Locate leukocytes (white blood cells).
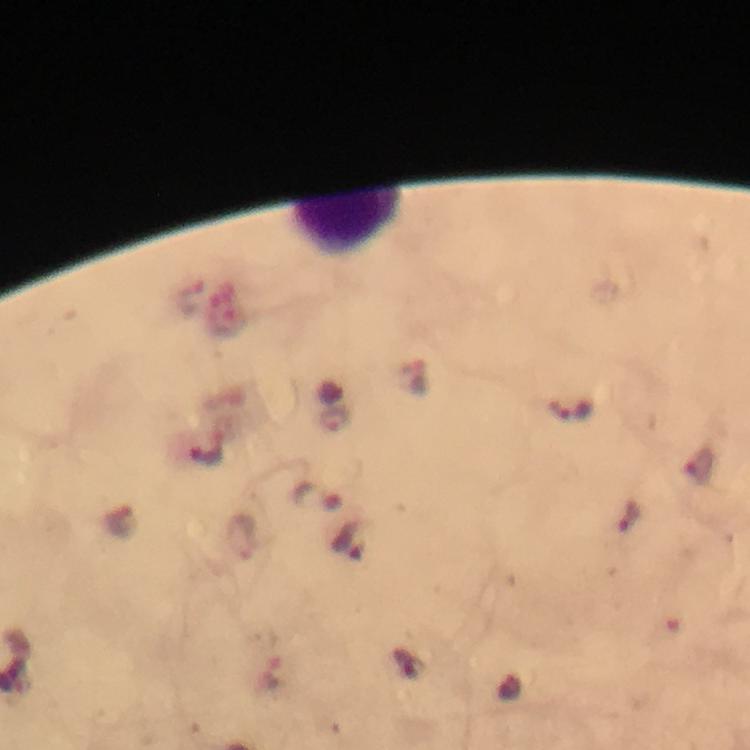

Approximate centers as (x, y) in pixels.
Leukocytes: (345, 229).

cropped_from: a single field of view
stain: Giemsa
image_size: 750×750 pixels
magnification: 100x
immersion_oil: used
malaria_parasite_locations: 'approximate centers as (x, y) in pixels: (569, 411), (335, 419), (317, 496), (239, 538)'
capture: smartphone camera through the microscope
context: from a malaria diagnostic workup
preparation: thick blood film